Locate every Plasmodium parasite.
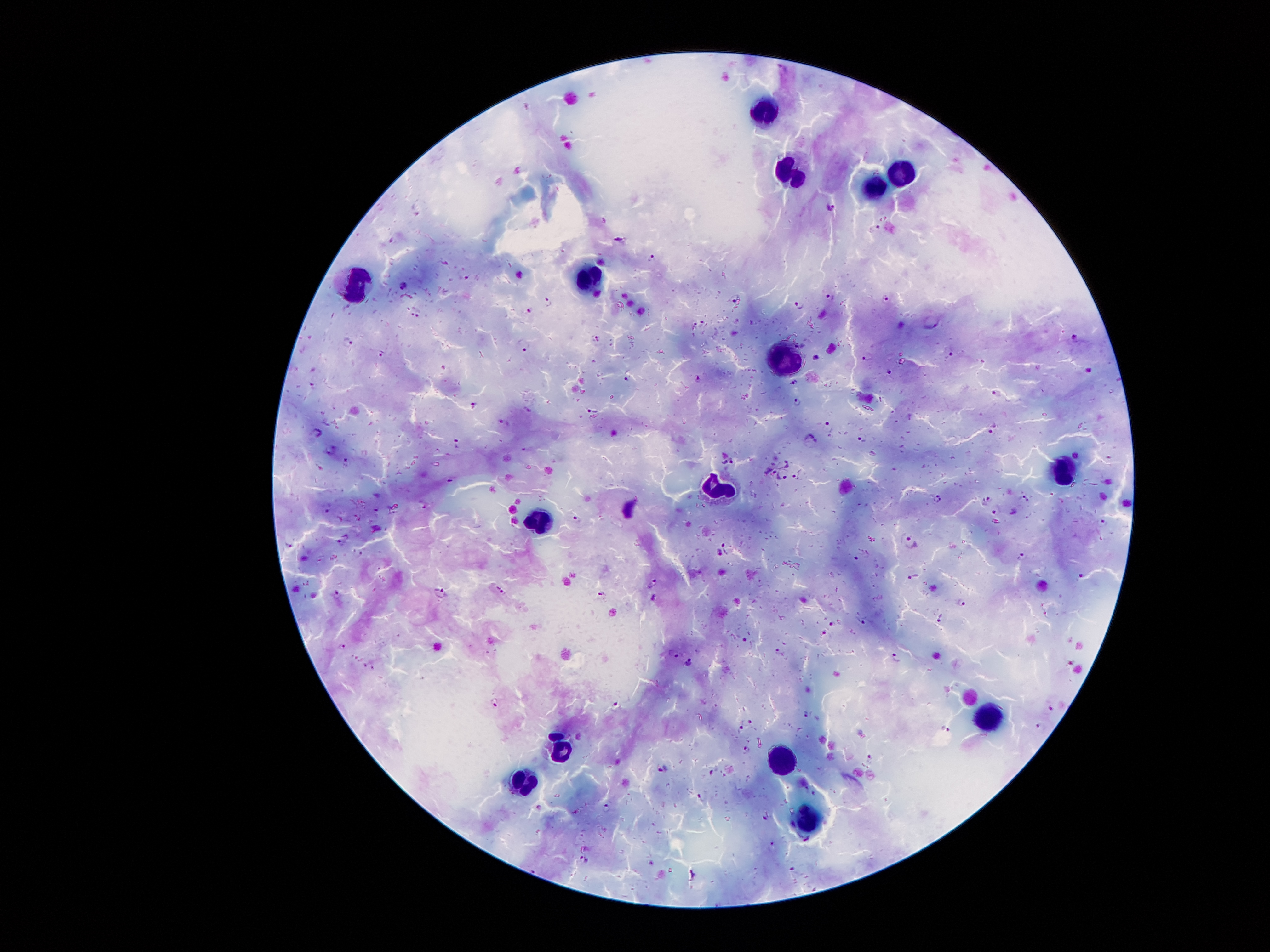
Approximate centers as (x, y) in pixels.
Plasmodium parasites: (783, 69), (832, 207), (652, 255), (519, 274), (406, 285), (828, 295), (736, 298), (886, 299), (548, 301), (798, 304), (529, 310), (417, 313), (933, 319), (1074, 334), (349, 342), (524, 346), (953, 353), (382, 354), (816, 356), (866, 356), (888, 370), (628, 373), (697, 379), (794, 381), (993, 393), (797, 402), (473, 404), (591, 406), (505, 422), (829, 427), (992, 429), (318, 432), (863, 436), (809, 440), (332, 449), (727, 459), (784, 459), (347, 463), (769, 470), (783, 474), (1025, 498), (936, 499), (986, 502), (329, 507), (996, 511), (577, 519), (342, 541), (911, 542), (290, 544), (721, 551), (1021, 555), (914, 575), (1080, 575), (654, 583), (500, 590), (439, 592), (337, 593), (653, 598), (961, 603), (940, 616), (833, 624), (823, 633), (745, 640), (342, 647), (673, 652), (778, 652), (895, 658), (690, 664), (494, 701), (616, 706), (1048, 709), (805, 714), (742, 723), (1040, 727), (945, 730), (746, 750), (869, 758), (665, 770), (702, 798), (607, 809), (768, 816), (809, 840), (772, 845), (585, 860), (692, 873).

{
  "capture": "smartphone camera through the microscope eyepiece",
  "leukocyte_locations": "approximate centers as (x, y) in pixels: (763, 112), (902, 167), (789, 171), (872, 185), (348, 281), (588, 290), (785, 359), (1065, 479), (718, 486), (533, 516), (990, 712), (561, 748), (785, 759), (530, 776), (810, 821)",
  "image_size": "1270×952 pixels",
  "field_of_view": "single",
  "patient_malaria_status": "infected with Plasmodium falciparum",
  "stain": "Giemsa",
  "magnification": "100x",
  "preparation": "thick blood film"
}